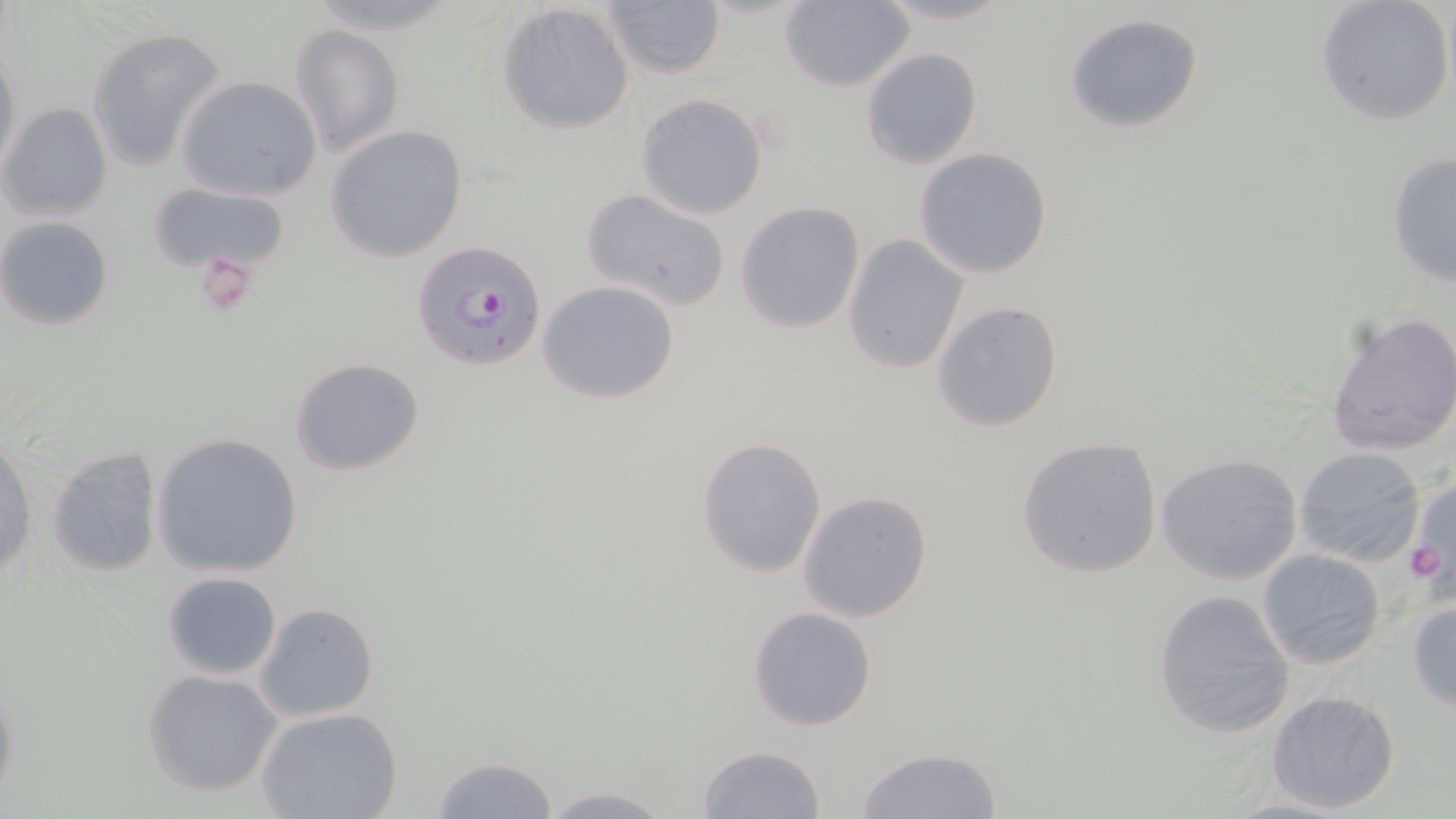

Summary:
  - Coordinate format: approximate bounding boxes as named x1/y1/x2/y2 corners in pixels
  - Platelet locations: (x1=189, y1=255, x2=256, y2=315), (x1=1406, y1=540, x2=1447, y2=585)
  - Uninfected red blood cell locations: (x1=496, y1=1, x2=637, y2=135), (x1=779, y1=1, x2=918, y2=91), (x1=1315, y1=1, x2=1455, y2=127), (x1=601, y1=2, x2=724, y2=81), (x1=1062, y1=13, x2=1207, y2=135), (x1=86, y1=24, x2=226, y2=172), (x1=290, y1=24, x2=405, y2=157), (x1=0, y1=42, x2=21, y2=178), (x1=861, y1=47, x2=982, y2=169), (x1=175, y1=76, x2=323, y2=201), (x1=635, y1=92, x2=769, y2=219), (x1=0, y1=102, x2=114, y2=223), (x1=324, y1=125, x2=470, y2=262), (x1=913, y1=148, x2=1056, y2=281), (x1=1386, y1=152, x2=1455, y2=287), (x1=149, y1=182, x2=291, y2=275), (x1=579, y1=187, x2=734, y2=310), (x1=736, y1=202, x2=865, y2=334), (x1=0, y1=216, x2=114, y2=329), (x1=842, y1=235, x2=970, y2=374), (x1=537, y1=279, x2=681, y2=404), (x1=932, y1=300, x2=1064, y2=433), (x1=1323, y1=310, x2=1456, y2=457), (x1=288, y1=355, x2=426, y2=476), (x1=152, y1=432, x2=304, y2=578), (x1=695, y1=435, x2=827, y2=579), (x1=1016, y1=435, x2=1164, y2=580), (x1=1, y1=439, x2=37, y2=581), (x1=44, y1=444, x2=165, y2=578), (x1=1293, y1=446, x2=1428, y2=567), (x1=1154, y1=452, x2=1304, y2=586), (x1=1408, y1=477, x2=1456, y2=596), (x1=795, y1=490, x2=935, y2=623), (x1=1257, y1=548, x2=1386, y2=669), (x1=161, y1=570, x2=282, y2=679), (x1=1153, y1=588, x2=1296, y2=739), (x1=1407, y1=597, x2=1456, y2=709), (x1=254, y1=602, x2=380, y2=721), (x1=748, y1=605, x2=878, y2=731), (x1=142, y1=669, x2=282, y2=797), (x1=1266, y1=688, x2=1401, y2=814), (x1=255, y1=707, x2=404, y2=819), (x1=697, y1=745, x2=826, y2=819), (x1=856, y1=746, x2=1004, y2=819), (x1=426, y1=754, x2=560, y2=818), (x1=534, y1=785, x2=681, y2=818)
  - Plasmodium falciparum-infected red blood cell locations: (x1=411, y1=237, x2=548, y2=370)
  - Slide-level diagnosis: Plasmodium falciparum
  - Preparation: thin blood film
  - Magnification: 1000x
  - Image size: 1456×819 pixels
  - Field of view: one of a larger specimen
  - Modality: optical microscopy
  - Stain: May-Grünwald-Giemsa